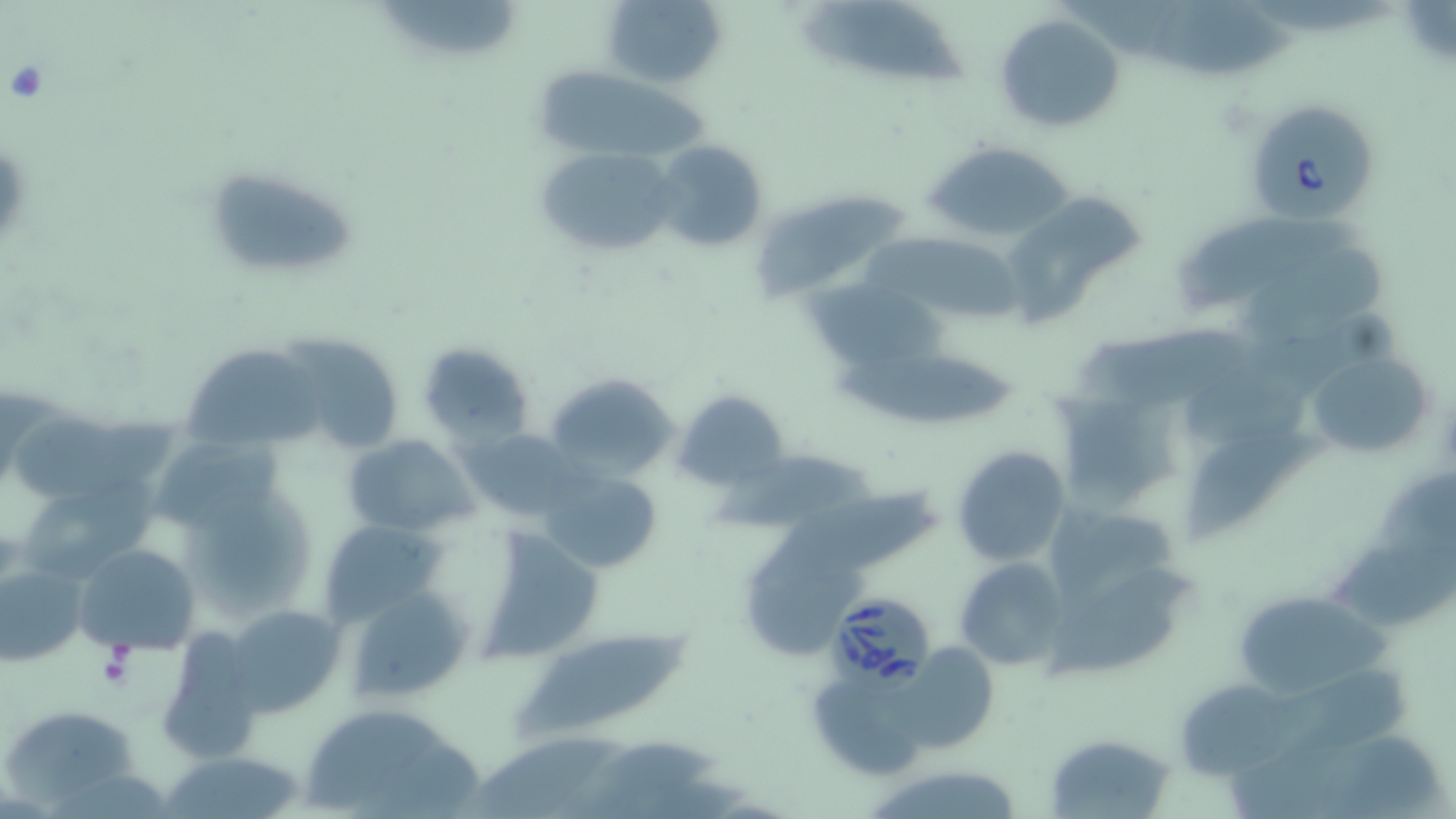
Babesia divergens-infected red blood cell locations = approximate bounding boxes as [x1, y1, x2, y2] in pixels: [1253, 96, 1378, 223], [827, 592, 934, 694]
slide-level diagnosis = Babesia divergens
uninfected red blood cell locations = approximate bounding boxes as [x1, y1, x2, y2] in pixels: [603, 0, 729, 89], [381, 1, 518, 55], [1150, 2, 1297, 81], [806, 3, 966, 90], [998, 12, 1125, 133], [534, 70, 721, 158], [653, 140, 769, 255], [925, 141, 1079, 245], [535, 145, 677, 259], [201, 164, 364, 284], [754, 195, 908, 297], [1005, 195, 1140, 324], [1173, 218, 1347, 313], [856, 231, 1026, 327], [1236, 247, 1393, 340], [794, 279, 952, 370], [1085, 320, 1258, 408], [292, 338, 403, 458], [417, 340, 534, 445], [187, 347, 327, 452], [1306, 348, 1433, 455], [832, 352, 1018, 426], [541, 373, 678, 484], [676, 391, 790, 491], [1056, 391, 1180, 502], [16, 412, 187, 502], [462, 428, 579, 523], [157, 433, 293, 535], [1186, 433, 1323, 541], [342, 434, 476, 535], [950, 445, 1070, 568], [716, 456, 876, 535], [541, 467, 665, 576], [19, 481, 168, 578], [752, 488, 942, 587], [185, 489, 320, 619], [1043, 503, 1182, 599], [315, 516, 447, 628], [483, 530, 608, 664], [1327, 537, 1456, 632], [75, 543, 202, 657], [954, 558, 1070, 672], [0, 560, 86, 666], [749, 563, 862, 664], [345, 587, 474, 703], [1054, 592, 1179, 685], [1229, 598, 1396, 701], [223, 605, 343, 716], [163, 625, 257, 765], [514, 633, 692, 738], [895, 639, 1002, 756], [1282, 665, 1427, 757], [1181, 685, 1323, 778], [294, 702, 484, 817], [4, 706, 140, 807], [1045, 732, 1175, 817], [462, 736, 622, 819], [161, 751, 306, 818], [861, 764, 1030, 819]
image size = 1456×819 pixels
magnification = 1000x
field of view = single
preparation = thin blood smear
stain = May-Grünwald-Giemsa
modality = light microscopy